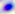 Toxoplasma gondii is shown. 400x magnification. Photomicrograph.